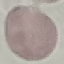
result = no malaria parasites detected
image type = cell patch, automatically extracted from a larger field of view and resized to 64 × 64 pixels
preparation = thin smear
stain = Giemsa
capture = smartphone camera at the microscope eyepiece